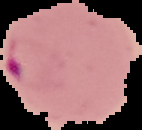 Cell region segmented out of the field of view; the surrounding area is masked to black. From a thin blood film. Image is 142×130 pixels. Malaria status: parasitized.